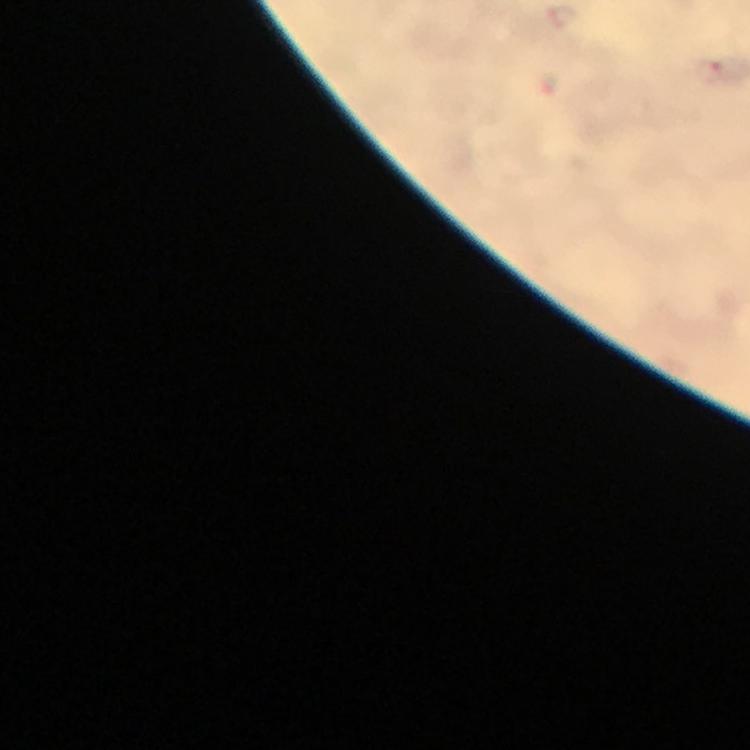

Approximate object centers, in pixels from the top-left corner.
Summary:
  - Malaria parasite locations: (x=710, y=72)
  - Capture: smartphone mounted on the microscope
  - Stain: Giemsa
  - Cropped from: a single field of view
  - Context: from a diagnostic examination for malaria
  - Immersion oil: used
  - Magnification: 100x
  - Image size: 750×750 pixels
  - Preparation: thick blood film